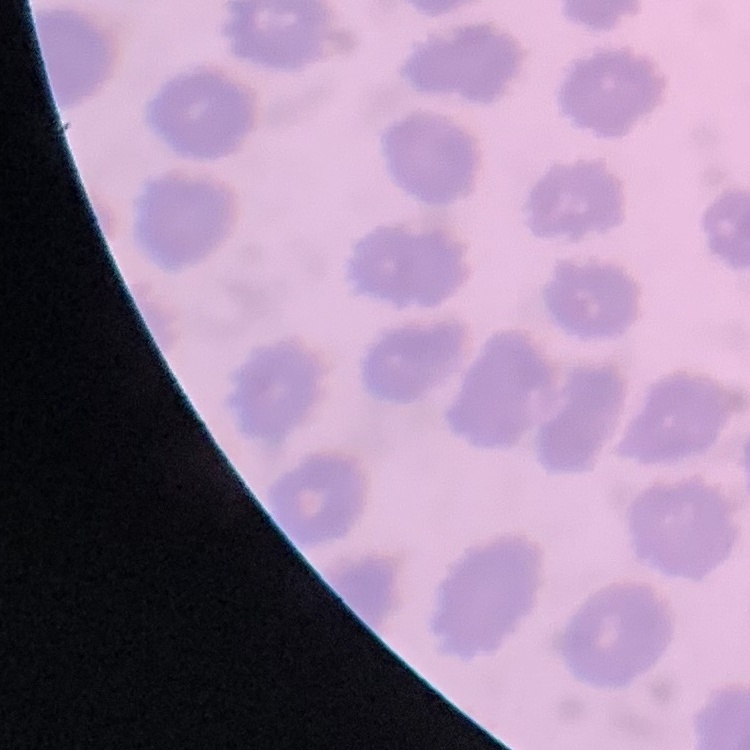

erythrocyte_morphology: no rouleaux formation
preparation: thin blood smear
image_type: one tile cut from a larger photomicrograph
stain: Field's or Giemsa